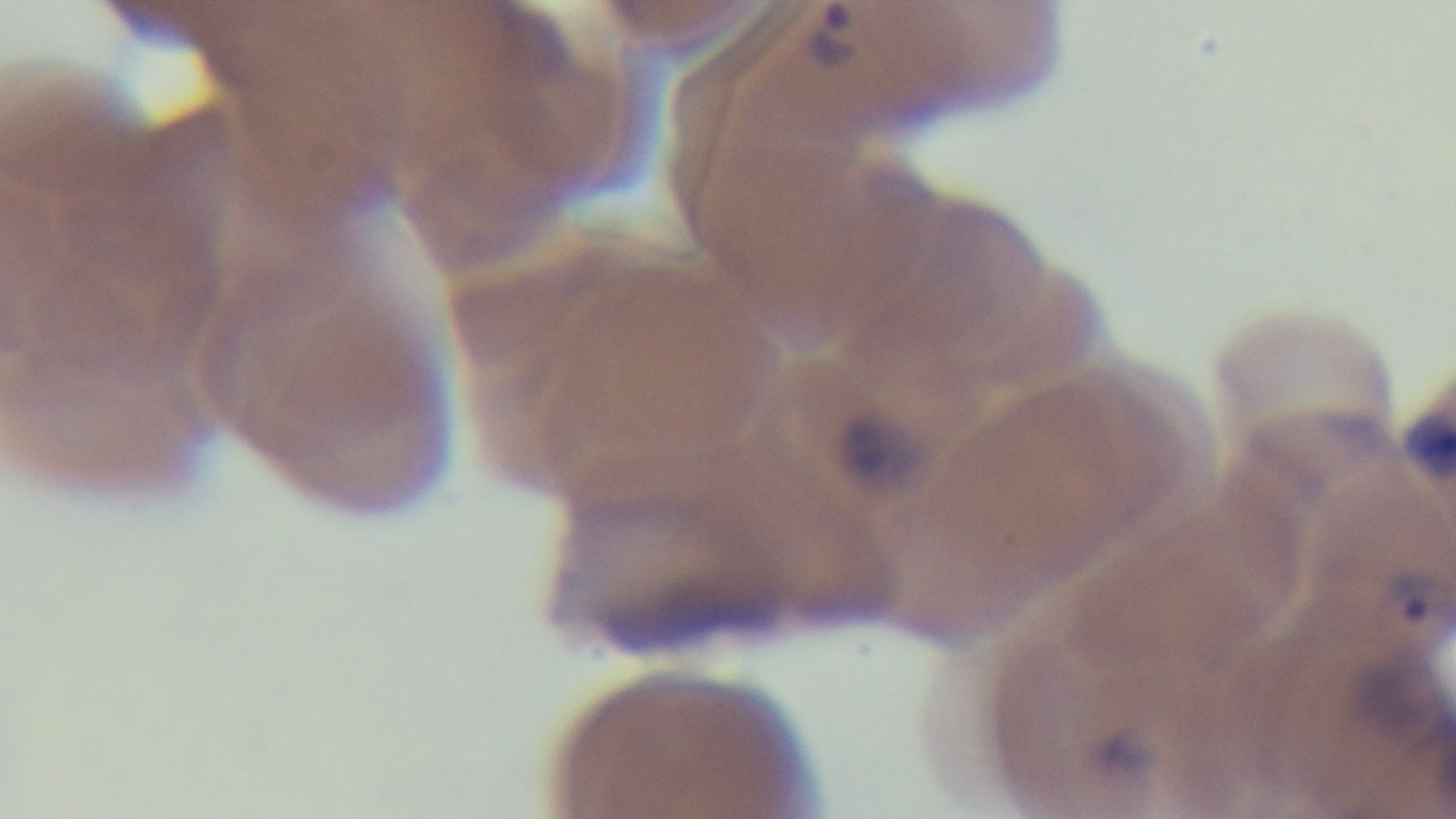

{
  "malaria_status": "infected",
  "field_of_view": "one from the slide",
  "modality": "light microscopy",
  "preparation": "thin blood film",
  "objective": "100x oil immersion",
  "capture": "mounted 4K digital camera",
  "stain": "Giemsa"
}